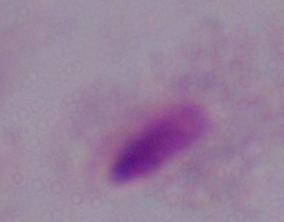
1000x magnification. A trichomonad is seen. Photomicrograph.